Classify this cell by malaria status.
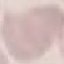
Uninfected.

image_type: automatically extracted cell patch, resized to 64 × 64 pixels
capture: smartphone through the microscope eyepiece
stain: Giemsa
preparation: thin blood film